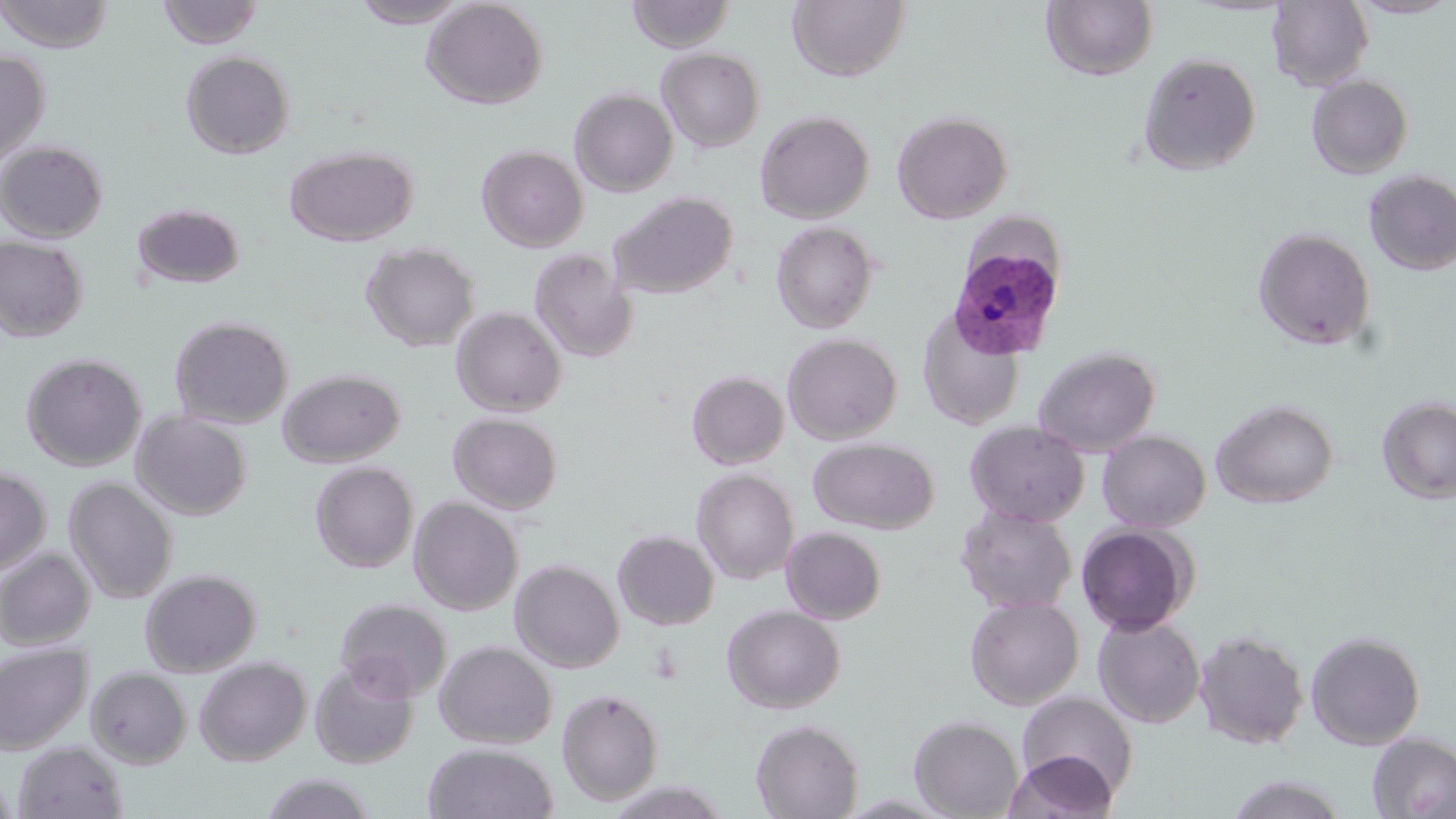
slide-level diagnosis = Plasmodium vivax
image size = 1456×819 pixels
modality = light microscopy
Plasmodium vivax-infected red blood cell locations = approximate bounding boxes as (x1,y1)-(x2,y2) corner pairs in pixels: (949,246)-(1064,359)
stain = May-Grünwald-Giemsa
preparation = thin blood film
uninfected red blood cell locations = approximate bounding boxes as (x1,y1)-(x2,y2) corner pairs in pixels: (0,0)-(114,53), (158,0)-(262,49), (350,0)-(474,28), (422,0)-(548,109), (627,0)-(735,53), (787,0)-(909,82), (1350,0)-(1456,19), (1041,1)-(1158,81), (1267,1)-(1374,91), (657,48)-(765,152), (0,49)-(50,171), (180,51)-(294,159), (1138,52)-(1261,175), (1306,74)-(1414,179), (569,88)-(678,197), (755,110)-(874,223), (892,111)-(1013,223), (0,141)-(108,243), (477,145)-(588,252), (285,146)-(417,247), (1363,169)-(1456,275), (609,191)-(737,298), (131,203)-(246,289), (771,221)-(879,334), (1252,227)-(1376,351), (0,236)-(87,342), (360,241)-(480,352), (529,248)-(638,363), (450,307)-(567,416), (917,307)-(1025,430), (169,316)-(293,429), (782,332)-(901,444), (1033,346)-(1160,457), (21,353)-(147,472), (277,368)-(406,467), (687,371)-(789,469), (1375,396)-(1456,505), (1211,399)-(1338,509), (131,410)-(251,520), (447,412)-(563,515), (964,420)-(1089,527), (1097,430)-(1211,532), (808,437)-(939,534), (310,461)-(418,573), (0,466)-(51,577), (692,469)-(798,584), (63,476)-(178,604), (408,496)-(523,615), (956,505)-(1077,615), (1076,523)-(1196,636), (781,527)-(886,625), (613,530)-(719,631), (0,548)-(95,650), (510,559)-(624,673), (140,568)-(261,677), (965,594)-(1084,710), (335,597)-(453,702), (722,604)-(845,714), (1093,614)-(1206,728), (1194,629)-(1308,749), (1306,630)-(1425,750), (434,640)-(557,748), (0,642)-(91,756), (195,657)-(311,765), (310,658)-(419,769), (86,666)-(192,769), (557,688)-(664,806), (1017,690)-(1138,798), (909,715)-(1024,818), (750,719)-(864,818), (1366,733)-(1456,818), (13,741)-(128,819), (423,743)-(559,819), (1002,751)-(1118,819), (0,770)-(18,819), (261,772)-(378,818), (1227,774)-(1347,818)
magnification = 1000x
field of view = single